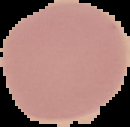 Image is 130×127 pixels. Malaria status: uninfected. Cell region segmented out of the field of view; the surrounding area is masked to black. From a thin blood smear.